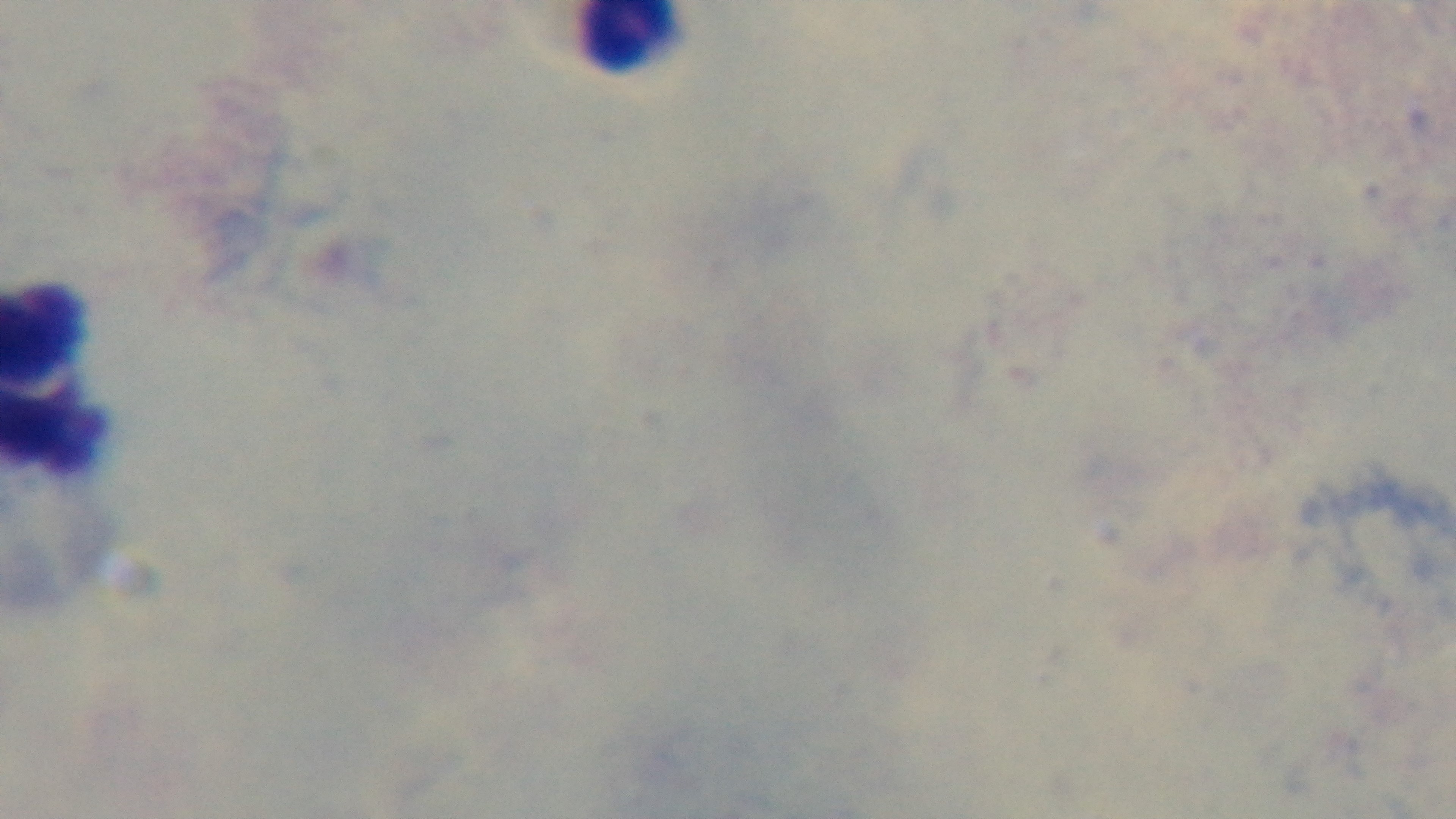

objective = 100x oil immersion
field of view = single
capture = mounted 4K digital camera
preparation = thick smear
malaria status = uninfected
modality = light microscopy
stain = Giemsa